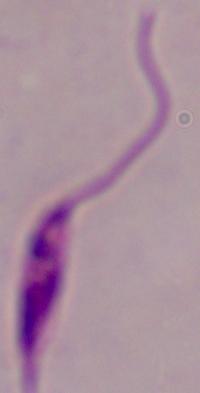
Summary:
  - Magnification: 1000x
  - Modality: photomicrograph
  - Identification: Leishmania